Identify the parasite.
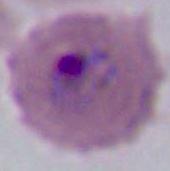
Plasmodium.

400x or 1000x magnification. Micrograph.